Report the malaria status of this cell.
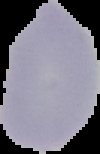
It is uninfected.

{
  "image_size": "100×154 pixels",
  "preparation": "thin blood smear",
  "image_type": "cell region segmented out of the field of view; surrounding area masked to black"
}